Evaluate for malaria.
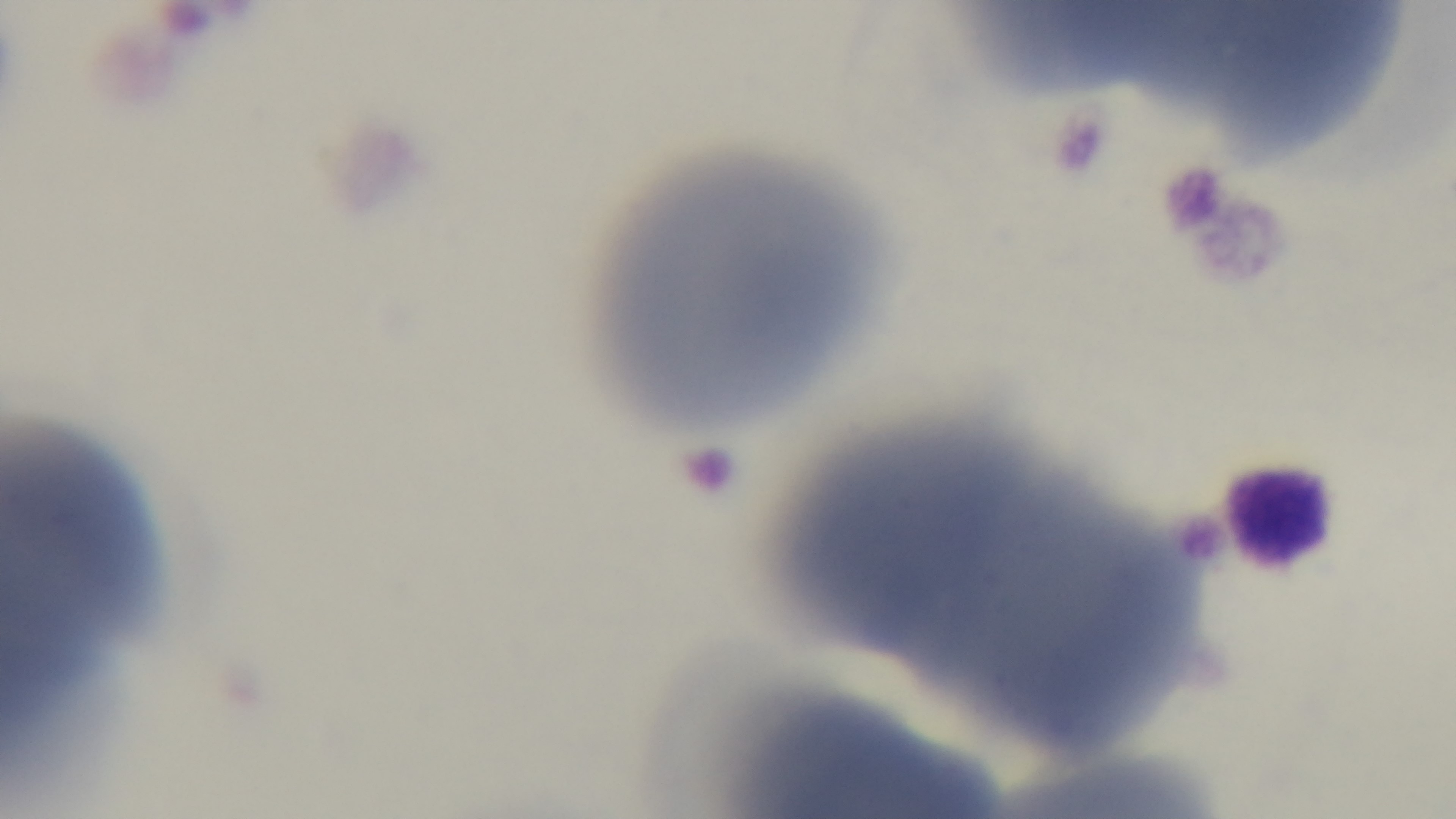
It is uninfected.

Summary:
  - Stain: Giemsa
  - Objective: 100x oil immersion
  - Field of view: one from the slide
  - Preparation: thin smear
  - Capture: mounted 4K digital camera
  - Modality: light microscopy